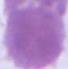
magnification = 1000x
modality = photomicrograph
identification = red blood cell